Give the location of every parasitized red blood cell.
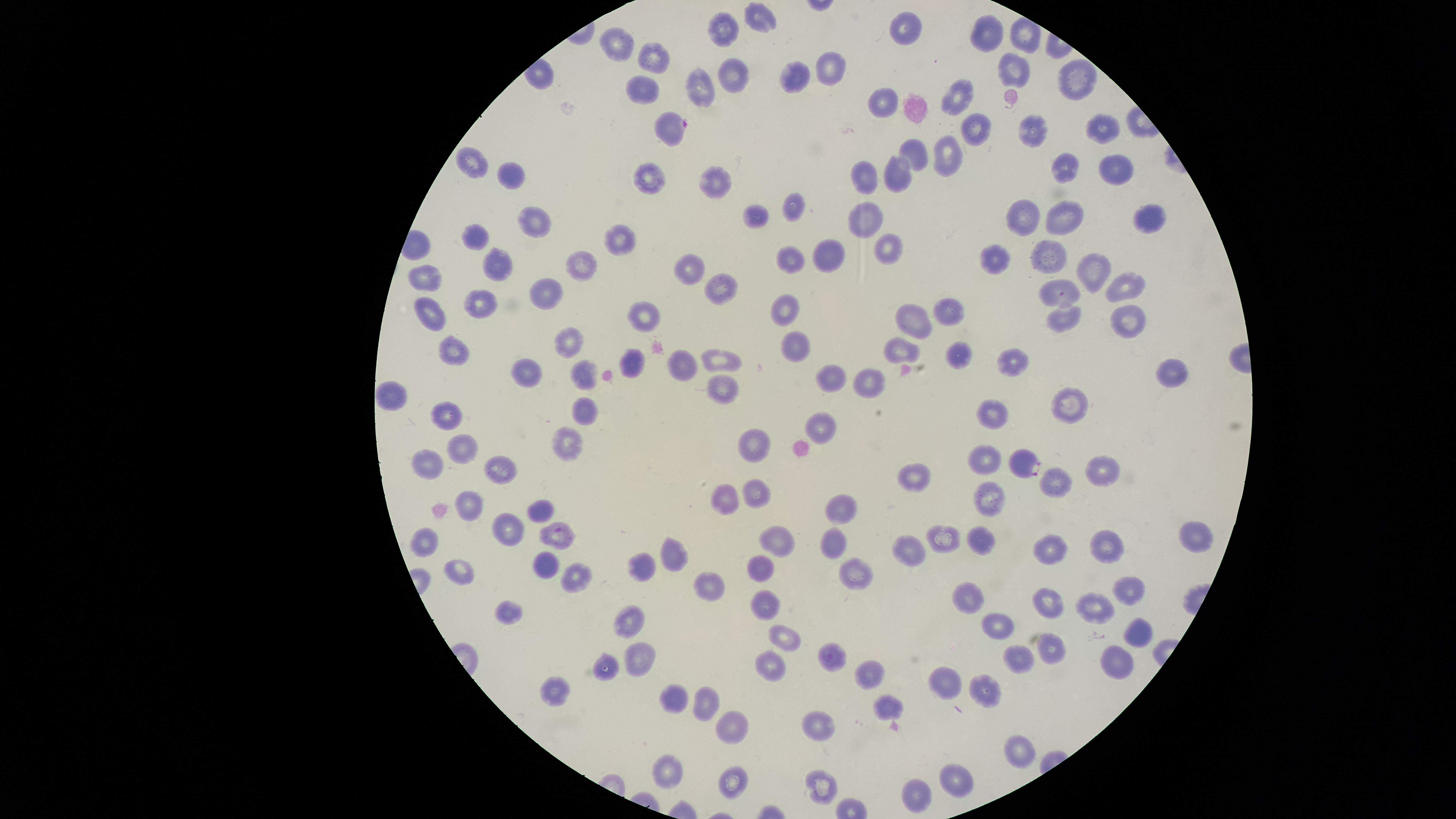

Approximate marker points as {x, y} in pixels.
Parasitized red blood cells: {674, 127}, {1024, 462}.

Approximate marker points as {x, y} in pixels.
Summary:
  - Uninfected red blood cells: {760, 18}, {726, 27}, {904, 27}, {993, 31}, {617, 45}, {651, 52}, {832, 64}, {1014, 69}, {734, 72}, {796, 77}, {1077, 79}, {701, 81}, {642, 85}, {885, 96}, {961, 98}, {974, 127}, {1031, 127}, {1098, 127}, {913, 152}, {947, 158}, {474, 161}, {1115, 164}, {1067, 167}, {900, 171}, {649, 175}, {868, 176}, {513, 177}, {713, 178}, {794, 205}, {758, 212}, {1027, 214}, {1065, 215}, {1149, 218}, {533, 221}, {862, 223}, {477, 233}, {620, 238}, {890, 248}, {1048, 255}, {830, 257}, {998, 257}, {579, 259}, {789, 259}, {495, 261}, {687, 268}, {1090, 269}, {426, 278}, {1125, 285}, {722, 288}, {544, 292}, {1060, 292}, {481, 301}, {786, 304}, {428, 312}, {947, 312}, {645, 315}, {1063, 315}, {911, 319}, {1128, 324}, {572, 340}, {796, 340}, {901, 346}, {454, 351}, {954, 354}, {719, 357}, {632, 361}, {1013, 362}, {1167, 369}, {523, 372}, {584, 372}, {830, 375}, {865, 379}, {721, 388}, {393, 395}, {1075, 401}, {996, 409}, {444, 412}, {583, 413}, {824, 423}, {565, 442}, {756, 442}, {464, 449}, {984, 456}, {429, 461}, {1098, 461}, {501, 471}, {914, 473}, {1054, 478}, {756, 488}, {727, 500}, {989, 500}, {470, 504}, {541, 507}, {842, 507}, {509, 528}, {1198, 535}, {557, 537}, {942, 538}, {425, 539}, {777, 541}, {985, 541}, {836, 542}, {1105, 546}, {1051, 548}, {910, 550}, {677, 559}, {541, 565}, {639, 565}, {759, 566}, {460, 567}, {856, 569}, {577, 577}, {711, 587}, {1126, 589}, {970, 598}, {764, 599}, {1051, 600}, {1093, 607}, {510, 610}, {630, 620}, {997, 624}, {1140, 630}, {784, 638}, {1050, 649}, {829, 656}, {1117, 659}, {637, 660}, {1022, 660}, {774, 661}, {608, 665}, {872, 670}, {949, 681}, {560, 688}, {992, 688}, {668, 699}, {703, 700}, {886, 708}, {735, 720}, {821, 726}, {1018, 745}, {671, 767}, {959, 779}, {732, 780}, {825, 781}, {918, 790}
  - Visible region: circular
  - Species: Plasmodium falciparum
  - Capture: smartphone photograph through the microscope eyepiece
  - Preparation: thin blood film
  - Image size: 1456×819 pixels
  - Field of view: single
  - Stain: Giemsa